Classify this cell by malaria status.
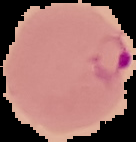

Parasitized.

preparation = thin blood smear
image type = segmented cell region on a black background
image size = 136×142 pixels